Locate and identify every blood parasite.
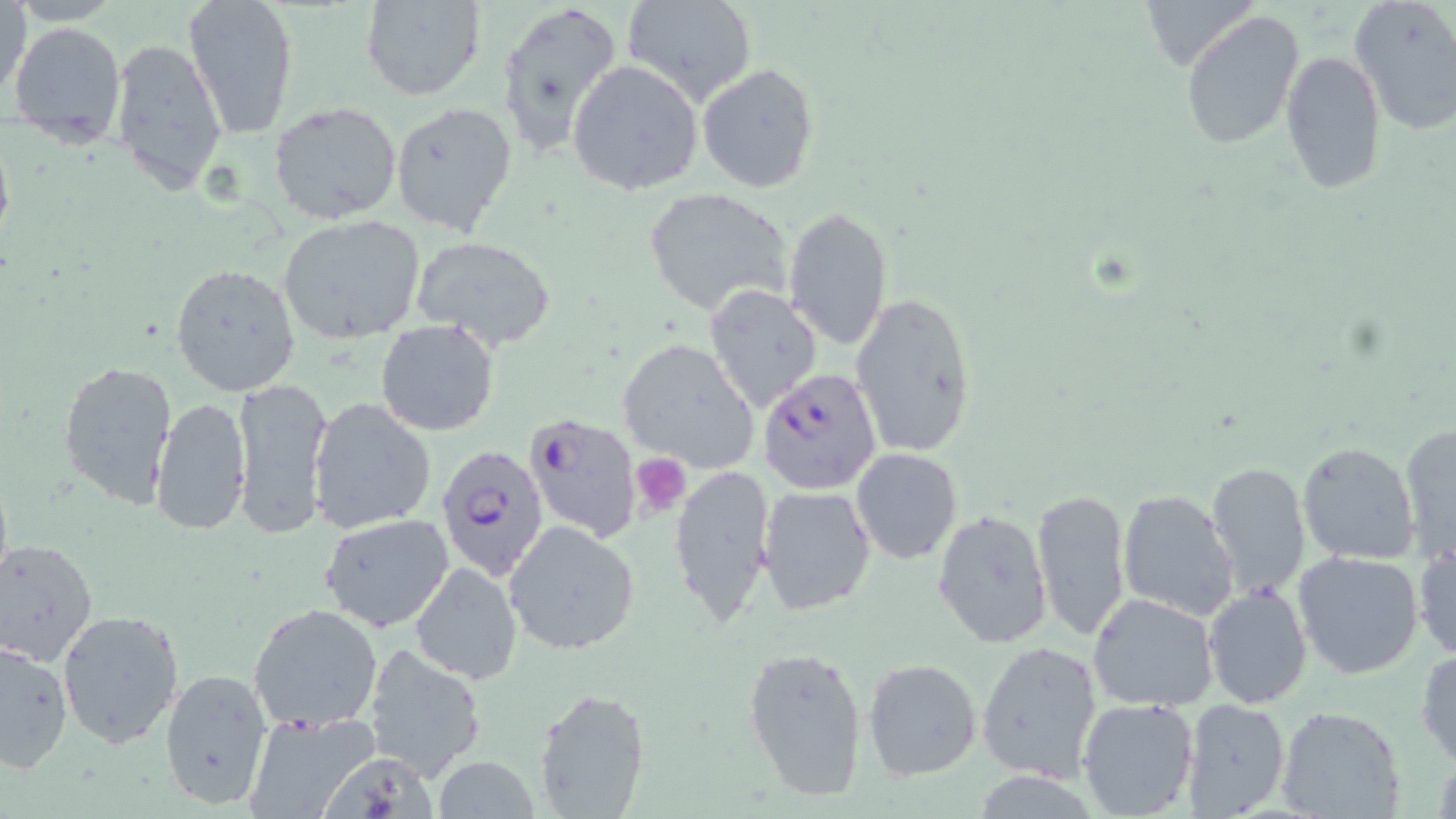

Approximate bounding boxes as [x1, y1, x2, y2] in pixels.
Plasmodium falciparum-infected red blood cells: [759, 368, 883, 494], [523, 411, 645, 544], [435, 444, 551, 582].
No Plasmodium ovale, Plasmodium malariae, Plasmodium vivax, Babesia divergens, or Trypanosoma brucei observed.

slide-level diagnosis = Plasmodium falciparum
platelet locations = approximate bounding boxes as [x1, y1, x2, y2] in pixels: [630, 454, 691, 514]
modality = light microscopy
preparation = thin blood film
image size = 1456×819 pixels
uninfected red blood cell locations = approximate bounding boxes as [x1, y1, x2, y2] in pixels: [1, 0, 31, 105], [184, 0, 299, 138], [497, 0, 624, 161], [620, 0, 759, 108], [1349, 0, 1456, 137], [359, 1, 486, 101], [1180, 9, 1304, 149], [8, 22, 126, 150], [108, 35, 229, 197], [1280, 51, 1386, 193], [569, 60, 704, 197], [698, 64, 819, 193], [268, 101, 402, 225], [389, 101, 518, 238], [642, 188, 792, 317], [783, 205, 894, 352], [277, 214, 425, 344], [410, 235, 557, 350], [171, 264, 301, 397], [704, 285, 823, 413], [849, 291, 978, 461], [375, 320, 501, 437], [616, 338, 759, 472], [57, 358, 177, 509], [230, 375, 332, 539], [149, 396, 252, 537], [309, 397, 437, 535], [1399, 423, 1456, 561], [1296, 441, 1422, 567], [850, 448, 962, 564], [667, 463, 776, 626], [1206, 463, 1313, 598], [757, 486, 877, 617], [1031, 488, 1132, 640], [1115, 489, 1240, 620], [932, 509, 1053, 649], [320, 513, 456, 633], [504, 519, 640, 656], [0, 540, 98, 666], [1412, 542, 1455, 661], [1293, 552, 1424, 680], [410, 561, 522, 685], [1202, 585, 1313, 710], [1088, 593, 1220, 712], [247, 602, 384, 734], [57, 607, 185, 748], [976, 641, 1104, 783], [0, 642, 73, 773], [362, 642, 486, 778], [742, 643, 870, 803], [1416, 648, 1456, 769], [862, 657, 983, 780], [159, 667, 273, 810], [534, 687, 652, 818], [1078, 697, 1200, 818], [1179, 698, 1290, 818], [1275, 706, 1406, 819], [242, 709, 380, 818], [322, 751, 437, 818], [433, 757, 542, 818]
stain = May-Grünwald-Giemsa
field of view = one of a larger specimen
magnification = 1000x